Name the cell type shown.
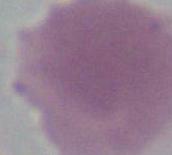
An erythrocyte.

Photomicrograph. Captured at 1000x magnification.